Name the cell type shown.
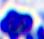

A leukocyte.

modality = micrograph
magnification = 400x